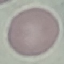 Malaria status: uninfected. Photographed with a smartphone camera at the microscope eyepiece. Thin smear of blood. Cell patch, automatically extracted from a larger field of view and resized to 64 × 64 pixels. Giemsa stain.